Name the blood parasite species.
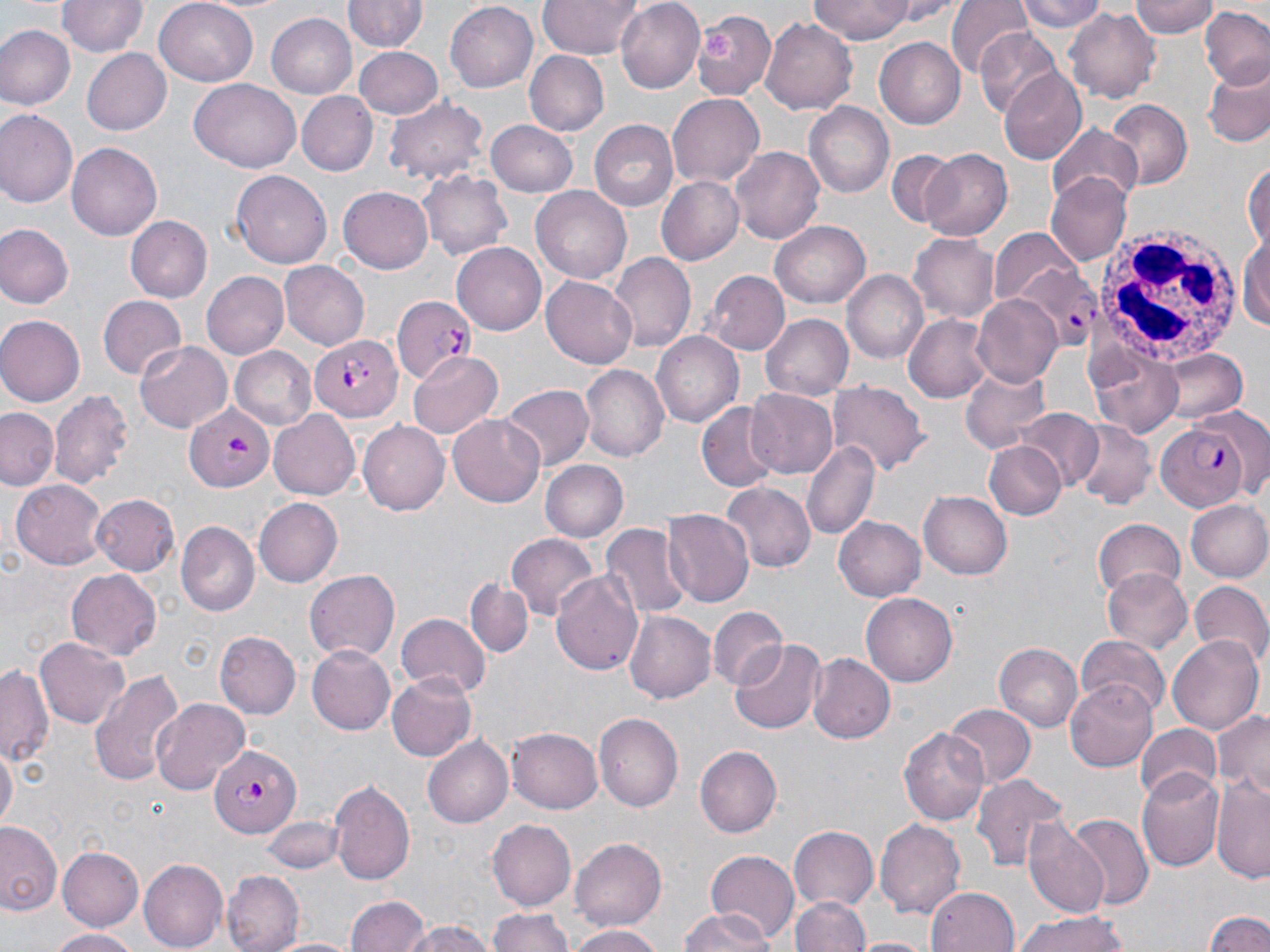
Plasmodium falciparum.

Summary:
  - Coordinate format: approximate bounding boxes as (x1, y1, x2, y2) in pixels
  - Platelet locations: (703, 29, 738, 64)
  - Uninfected red blood cell locations: (60, 0, 146, 58), (153, 0, 258, 86), (539, 0, 641, 59), (613, 0, 703, 91), (808, 0, 918, 42), (1018, 0, 1109, 32), (1131, 0, 1219, 39), (345, 1, 426, 53), (948, 1, 1032, 79), (447, 3, 538, 92), (1200, 6, 1270, 90), (1068, 8, 1161, 104), (691, 9, 775, 100), (265, 12, 357, 98), (761, 19, 857, 113), (2, 26, 74, 109), (975, 30, 1067, 117), (876, 39, 965, 128), (80, 46, 171, 135), (354, 46, 443, 120), (523, 50, 608, 136), (1203, 64, 1270, 148), (997, 71, 1086, 166), (188, 79, 301, 172), (298, 93, 376, 175), (668, 93, 764, 186), (386, 95, 489, 184), (1104, 100, 1191, 189), (804, 103, 893, 199), (0, 109, 78, 207), (486, 119, 578, 197), (590, 119, 680, 211), (1048, 125, 1143, 207), (67, 143, 163, 240), (883, 144, 969, 231), (732, 147, 826, 243), (920, 148, 1013, 240), (1243, 159, 1269, 252), (229, 169, 331, 268), (420, 170, 512, 263), (1045, 173, 1132, 266), (655, 176, 744, 264), (338, 186, 435, 274), (531, 187, 631, 286), (126, 216, 211, 302), (770, 222, 871, 308), (0, 224, 73, 307), (1242, 227, 1270, 335), (990, 230, 1084, 307), (911, 232, 1001, 322), (453, 241, 547, 333), (609, 253, 696, 350), (280, 262, 369, 351), (201, 269, 289, 357), (842, 269, 926, 364), (706, 271, 790, 355), (542, 276, 637, 369), (971, 292, 1066, 387), (98, 295, 186, 380), (904, 312, 998, 403), (761, 314, 855, 400), (0, 315, 84, 407), (650, 331, 745, 428), (136, 342, 231, 432), (1087, 346, 1184, 438), (232, 347, 316, 429), (1154, 348, 1249, 425), (408, 351, 502, 440), (582, 364, 669, 462), (961, 364, 1050, 452), (829, 383, 930, 475), (500, 384, 593, 471), (745, 387, 839, 478), (49, 388, 133, 491), (696, 403, 780, 492), (0, 408, 60, 489), (269, 410, 363, 499), (1015, 410, 1103, 490), (448, 415, 547, 508), (1069, 417, 1158, 509), (358, 421, 448, 516), (801, 440, 880, 539), (984, 440, 1066, 521), (539, 459, 628, 543), (10, 476, 105, 565), (721, 482, 815, 573), (919, 491, 1011, 579), (92, 492, 180, 575), (255, 499, 341, 587), (1185, 499, 1270, 583), (662, 508, 753, 606), (835, 517, 926, 601), (1091, 519, 1185, 598), (177, 522, 257, 617), (602, 523, 692, 617), (508, 533, 600, 619), (1103, 568, 1193, 656), (67, 569, 162, 661), (305, 569, 400, 662), (553, 570, 644, 674), (464, 575, 534, 657), (1188, 583, 1270, 671), (863, 594, 957, 685), (710, 607, 789, 688), (624, 608, 719, 703), (395, 613, 491, 697), (216, 631, 300, 717), (1168, 633, 1264, 735), (1075, 635, 1170, 717), (36, 639, 129, 727), (731, 639, 825, 734), (310, 643, 399, 734), (994, 644, 1082, 734), (808, 653, 893, 744), (0, 665, 55, 767), (90, 668, 182, 787), (389, 670, 478, 761), (1066, 681, 1162, 772), (152, 698, 249, 793), (945, 703, 1035, 788), (1215, 709, 1270, 798), (595, 713, 684, 811), (1135, 722, 1220, 803), (898, 724, 991, 827), (508, 726, 605, 813), (423, 735, 514, 828), (694, 746, 781, 837), (0, 748, 15, 832), (1136, 770, 1224, 873), (973, 773, 1070, 876), (1212, 778, 1270, 882), (330, 779, 416, 888), (1062, 813, 1153, 913), (875, 816, 965, 919), (263, 817, 343, 874), (1026, 818, 1112, 920), (489, 820, 575, 907), (0, 821, 63, 918), (787, 827, 879, 913), (571, 836, 669, 930), (56, 844, 145, 929), (705, 849, 799, 942), (140, 859, 226, 949), (223, 872, 302, 952), (925, 885, 1021, 952), (345, 894, 430, 952), (793, 895, 871, 952), (486, 908, 578, 952), (678, 909, 771, 952), (1200, 909, 1270, 952), (1010, 911, 1136, 952), (398, 919, 500, 952), (567, 925, 664, 952), (47, 928, 140, 952), (267, 936, 361, 952), (854, 937, 930, 952)
  - White blood cell locations: (1093, 222, 1245, 370)
  - Plasmodium falciparum-infected red blood cell locations: (1009, 259, 1100, 350), (392, 296, 477, 385), (310, 333, 402, 423), (183, 404, 277, 490), (1157, 414, 1256, 509), (210, 742, 300, 836)
  - Magnification: 1000x
  - Stain: May-Grünwald-Giemsa
  - Image size: 1270×952 pixels
  - Preparation: thin blood smear
  - Field of view: single
  - Modality: optical microscopy